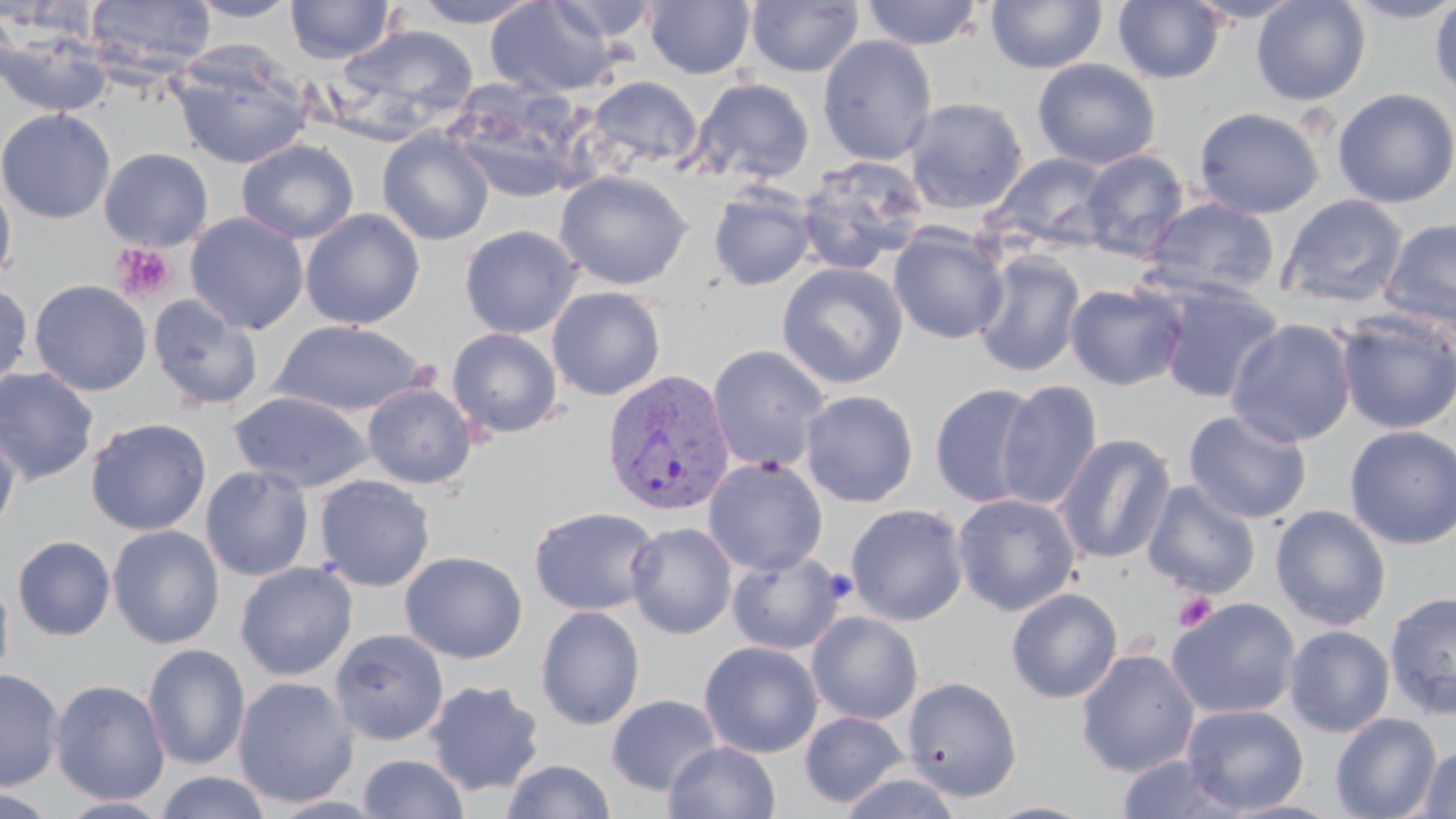
Summary:
  - Coordinate format: approximate bounding boxes as named x1/y1/x2/y2 corners in pixels
  - Platelet locations: (x1=110, y1=243, x2=177, y2=302), (x1=1173, y1=592, x2=1217, y2=633)
  - Plasmodium vivax-infected red blood cell locations: (x1=601, y1=369, x2=735, y2=516)
  - Uninfected red blood cell locations: (x1=86, y1=0, x2=217, y2=77), (x1=185, y1=0, x2=302, y2=23), (x1=285, y1=0, x2=396, y2=64), (x1=409, y1=0, x2=543, y2=27), (x1=546, y1=0, x2=661, y2=42), (x1=644, y1=0, x2=755, y2=78), (x1=746, y1=0, x2=864, y2=78), (x1=985, y1=0, x2=1107, y2=74), (x1=1113, y1=0, x2=1226, y2=84), (x1=1183, y1=0, x2=1307, y2=24), (x1=1250, y1=0, x2=1371, y2=106), (x1=1341, y1=0, x2=1456, y2=24), (x1=486, y1=1, x2=619, y2=98), (x1=860, y1=1, x2=985, y2=50), (x1=1429, y1=1, x2=1456, y2=98), (x1=331, y1=24, x2=479, y2=142), (x1=0, y1=27, x2=113, y2=117), (x1=817, y1=35, x2=938, y2=166), (x1=171, y1=50, x2=313, y2=170), (x1=1032, y1=58, x2=1160, y2=170), (x1=585, y1=75, x2=703, y2=171), (x1=688, y1=77, x2=815, y2=185), (x1=444, y1=79, x2=589, y2=204), (x1=1332, y1=88, x2=1456, y2=209), (x1=903, y1=97, x2=1029, y2=215), (x1=1193, y1=107, x2=1324, y2=219), (x1=0, y1=108, x2=116, y2=224), (x1=377, y1=127, x2=495, y2=246), (x1=237, y1=139, x2=359, y2=244), (x1=99, y1=148, x2=214, y2=251), (x1=1080, y1=150, x2=1189, y2=261), (x1=989, y1=152, x2=1114, y2=252), (x1=797, y1=156, x2=929, y2=273), (x1=553, y1=170, x2=693, y2=290), (x1=0, y1=179, x2=17, y2=287), (x1=708, y1=185, x2=817, y2=291), (x1=1279, y1=194, x2=1408, y2=309), (x1=1142, y1=196, x2=1280, y2=299), (x1=300, y1=208, x2=425, y2=330), (x1=185, y1=212, x2=309, y2=335), (x1=1380, y1=219, x2=1456, y2=331), (x1=459, y1=225, x2=582, y2=338), (x1=888, y1=228, x2=1009, y2=345), (x1=973, y1=251, x2=1085, y2=377), (x1=776, y1=262, x2=909, y2=389), (x1=29, y1=279, x2=152, y2=396), (x1=0, y1=281, x2=33, y2=395), (x1=1064, y1=282, x2=1187, y2=391), (x1=1155, y1=282, x2=1284, y2=404), (x1=547, y1=286, x2=666, y2=401), (x1=147, y1=294, x2=264, y2=412), (x1=1335, y1=312, x2=1456, y2=434), (x1=1226, y1=319, x2=1357, y2=447), (x1=272, y1=320, x2=429, y2=417), (x1=446, y1=328, x2=564, y2=439), (x1=707, y1=344, x2=831, y2=474), (x1=0, y1=367, x2=99, y2=486), (x1=995, y1=381, x2=1103, y2=511), (x1=929, y1=382, x2=1044, y2=509), (x1=362, y1=383, x2=478, y2=489), (x1=229, y1=390, x2=375, y2=492), (x1=800, y1=390, x2=919, y2=507), (x1=1183, y1=409, x2=1313, y2=524), (x1=85, y1=417, x2=212, y2=536), (x1=0, y1=422, x2=21, y2=539), (x1=1344, y1=425, x2=1456, y2=550), (x1=1054, y1=433, x2=1176, y2=565), (x1=703, y1=457, x2=828, y2=576), (x1=200, y1=465, x2=315, y2=581), (x1=314, y1=475, x2=436, y2=591), (x1=1141, y1=479, x2=1261, y2=599), (x1=951, y1=493, x2=1081, y2=616), (x1=845, y1=503, x2=969, y2=626), (x1=529, y1=505, x2=660, y2=616), (x1=1270, y1=505, x2=1392, y2=630), (x1=625, y1=521, x2=737, y2=639), (x1=108, y1=524, x2=225, y2=649), (x1=12, y1=535, x2=116, y2=641), (x1=400, y1=551, x2=527, y2=663), (x1=727, y1=553, x2=846, y2=654), (x1=235, y1=561, x2=358, y2=681), (x1=0, y1=569, x2=14, y2=691), (x1=1006, y1=588, x2=1123, y2=704), (x1=1384, y1=591, x2=1456, y2=720), (x1=1166, y1=597, x2=1302, y2=720), (x1=535, y1=606, x2=646, y2=730), (x1=807, y1=611, x2=923, y2=725), (x1=1284, y1=625, x2=1395, y2=737), (x1=330, y1=628, x2=448, y2=745), (x1=699, y1=641, x2=823, y2=758), (x1=142, y1=644, x2=250, y2=770), (x1=1076, y1=648, x2=1201, y2=777), (x1=0, y1=668, x2=65, y2=791), (x1=232, y1=676, x2=359, y2=809), (x1=902, y1=676, x2=1022, y2=801), (x1=50, y1=679, x2=170, y2=805), (x1=424, y1=680, x2=545, y2=796), (x1=607, y1=694, x2=721, y2=796), (x1=1181, y1=703, x2=1309, y2=814), (x1=799, y1=711, x2=910, y2=808), (x1=1330, y1=713, x2=1442, y2=819), (x1=665, y1=741, x2=781, y2=819), (x1=1418, y1=745, x2=1456, y2=818), (x1=358, y1=753, x2=469, y2=818), (x1=1115, y1=754, x2=1247, y2=818), (x1=500, y1=759, x2=617, y2=819), (x1=153, y1=771, x2=273, y2=819), (x1=837, y1=771, x2=965, y2=818), (x1=0, y1=784, x2=64, y2=817), (x1=57, y1=795, x2=174, y2=818), (x1=982, y1=801, x2=1100, y2=819)
  - Slide-level diagnosis: Plasmodium vivax
  - Magnification: 1000x
  - Field of view: one of a larger specimen
  - Stain: May-Grünwald-Giemsa
  - Modality: light microscopy
  - Preparation: thin blood smear
  - Image size: 1456×819 pixels